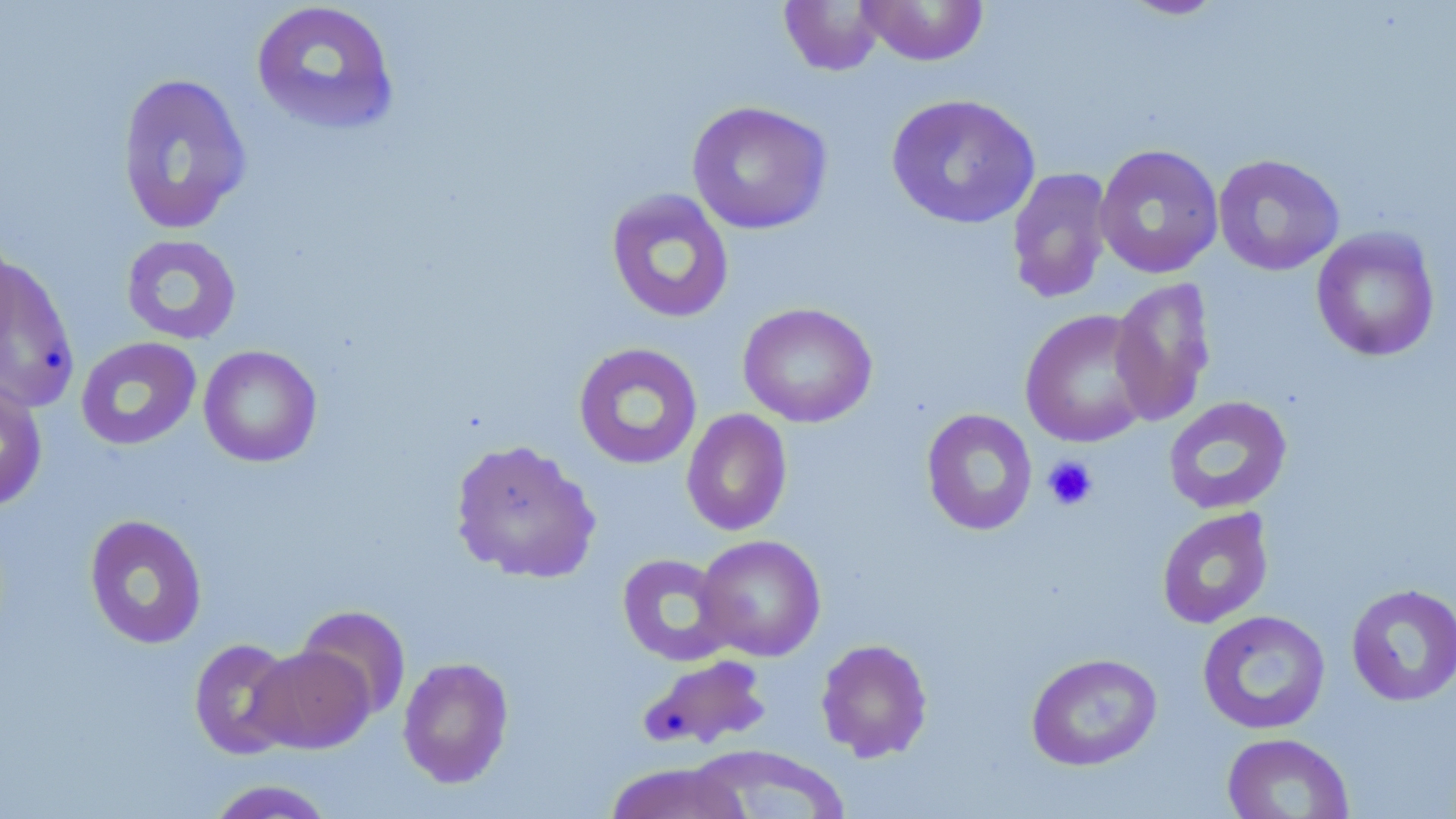

Approximate bounding boxes as (x1,y1)-(x2,y2) corner pairs in pixels. Platelet locations: (1043,455)-(1098,511). Uninfected red blood cell locations: (857,0)-(990,66), (1117,0)-(1229,20), (250,1)-(400,136), (779,1)-(887,76), (116,72)-(253,235), (886,93)-(1041,230), (687,101)-(832,235), (1094,144)-(1224,279), (1213,154)-(1345,276), (1006,167)-(1114,304), (605,188)-(735,324), (1311,227)-(1441,362), (121,234)-(242,345), (0,256)-(80,414), (1109,277)-(1217,426), (738,302)-(877,428), (1020,308)-(1156,448), (75,336)-(202,451), (573,342)-(703,470), (198,345)-(323,467), (0,379)-(49,511), (1163,396)-(1292,515), (921,408)-(1038,536), (681,409)-(793,537), (449,438)-(601,584), (1156,507)-(1274,629), (83,514)-(208,649), (695,534)-(826,661), (616,552)-(738,666), (1345,583)-(1456,707), (295,604)-(411,721), (1197,609)-(1331,735), (188,637)-(302,759), (815,638)-(933,762), (248,645)-(374,753), (1025,652)-(1163,771), (637,654)-(772,751), (397,656)-(514,788), (1221,732)-(1355,819), (688,745)-(851,818), (603,762)-(752,819), (203,779)-(338,819). Slide-level diagnosis: negative for blood parasites. Thin blood film. Image is 1456×819 pixels. Optical microscopy. 1000x magnification. May-Grünwald-Giemsa-stained preparation. Single field of view.